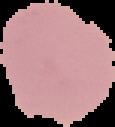
Summary:
  - Result: no malaria parasites detected
  - Image type: segmented cell region with the area outside set to black
  - Image size: 115×127 pixels
  - Preparation: thin blood film